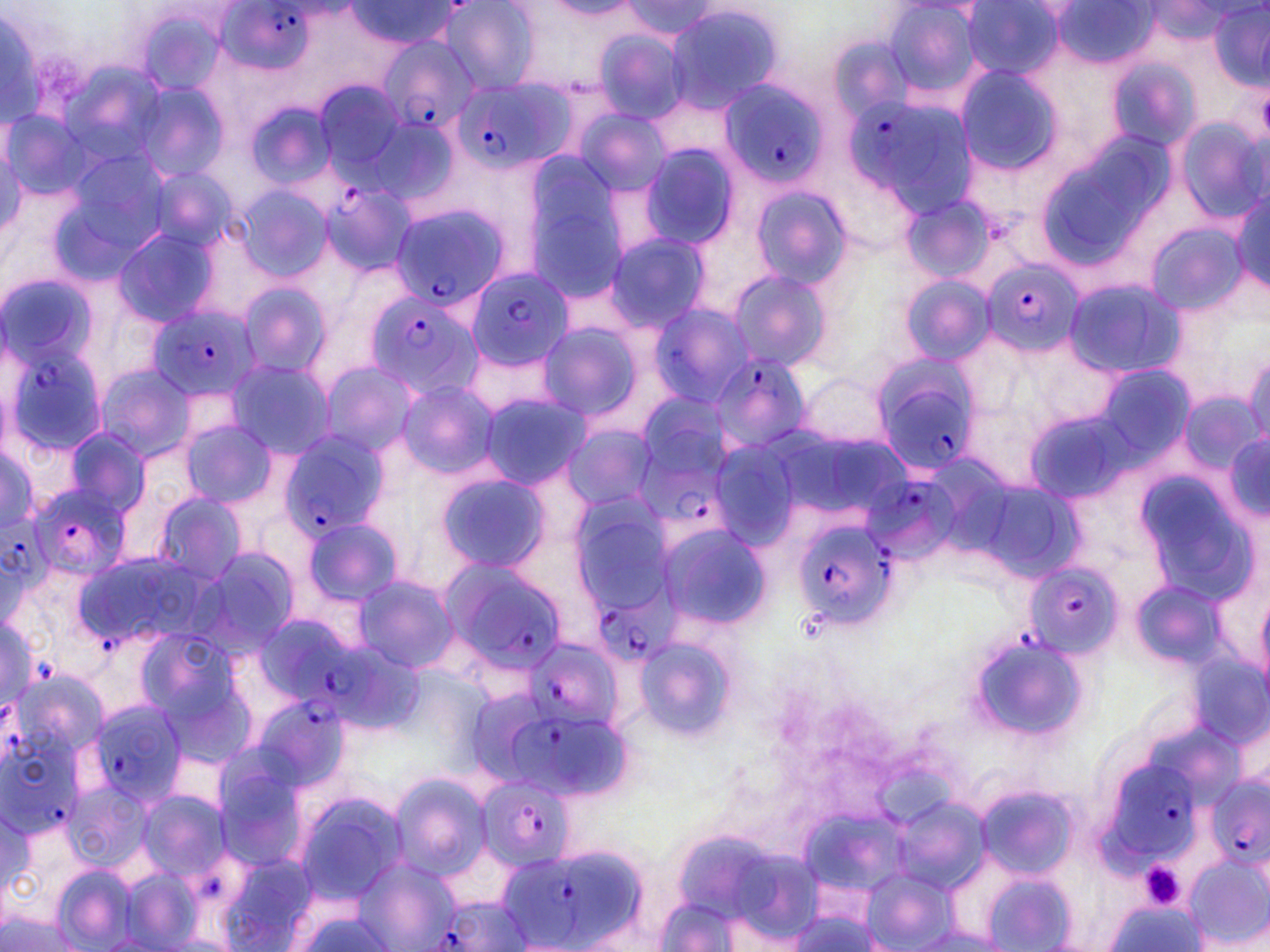
Summary:
  - Coordinate format: approximate bounding boxes as (x1, y1, x2, y2) in pixels
  - Plasmodium falciparum-infected red blood cell locations: (216, 0, 314, 74), (375, 32, 480, 141), (720, 78, 829, 192), (454, 79, 567, 174), (848, 94, 971, 214), (324, 182, 414, 276), (387, 204, 509, 311), (982, 255, 1081, 361), (464, 267, 573, 370), (364, 289, 482, 401), (148, 305, 256, 402), (3, 339, 101, 463), (706, 350, 812, 455), (867, 360, 978, 475), (638, 426, 730, 520), (278, 434, 389, 540), (861, 479, 967, 565), (30, 481, 128, 581), (792, 511, 904, 633), (1, 519, 54, 595), (441, 559, 567, 674), (1025, 562, 1121, 662), (590, 563, 681, 666), (529, 643, 619, 737), (289, 644, 376, 721), (254, 697, 347, 788), (87, 701, 187, 805), (510, 713, 609, 798), (0, 742, 82, 837), (1109, 763, 1197, 861), (1208, 772, 1269, 869), (478, 775, 575, 870), (497, 844, 655, 951), (435, 896, 528, 950)
  - Uninfected red blood cell locations: (340, 0, 462, 52), (441, 0, 541, 95), (621, 1, 723, 40), (882, 1, 981, 99), (960, 2, 1070, 84), (1208, 2, 1270, 87), (662, 4, 781, 112), (2, 8, 46, 134), (137, 11, 220, 92), (592, 29, 692, 123), (1099, 54, 1201, 156), (959, 67, 1059, 172), (310, 78, 409, 178), (137, 81, 227, 185), (246, 101, 337, 193), (3, 106, 91, 205), (574, 107, 672, 199), (1176, 115, 1266, 222), (639, 144, 738, 251), (147, 162, 236, 260), (523, 170, 633, 304), (235, 181, 332, 285), (748, 183, 852, 290), (1227, 191, 1270, 295), (899, 194, 996, 287), (1147, 219, 1248, 317), (111, 226, 220, 331), (604, 233, 710, 333), (733, 268, 832, 372), (899, 275, 994, 367), (1064, 278, 1183, 379), (239, 282, 333, 383), (648, 303, 758, 409), (532, 320, 646, 425), (1243, 352, 1270, 449), (223, 358, 334, 460), (315, 360, 419, 460), (95, 364, 194, 463), (795, 371, 895, 452), (395, 379, 499, 479), (632, 389, 737, 477), (477, 391, 589, 491), (181, 421, 276, 508), (563, 423, 659, 513), (62, 427, 150, 516), (1226, 434, 1270, 520), (0, 443, 42, 535), (433, 471, 549, 576), (149, 491, 247, 586), (561, 495, 681, 620), (301, 516, 403, 609), (656, 524, 768, 631), (198, 548, 300, 655), (352, 572, 458, 675), (1132, 577, 1226, 669), (635, 636, 734, 742), (391, 774, 492, 879), (977, 786, 1074, 879), (139, 791, 229, 882), (292, 791, 408, 907), (1, 808, 32, 896), (1187, 854, 1268, 948), (355, 856, 457, 952), (861, 870, 953, 947), (122, 871, 204, 946), (982, 874, 1074, 948), (655, 897, 736, 950), (1110, 902, 1198, 951), (288, 911, 398, 952)
  - Platelet locations: (1144, 865, 1183, 904)
  - Slide-level diagnosis: Plasmodium falciparum
  - Modality: optical microscopy
  - Magnification: 1000x
  - Field of view: single
  - Image size: 1270×952 pixels
  - Preparation: thin blood film
  - Stain: May-Grünwald-Giemsa